Point out each Plasmodium parasite and each leukocyte.
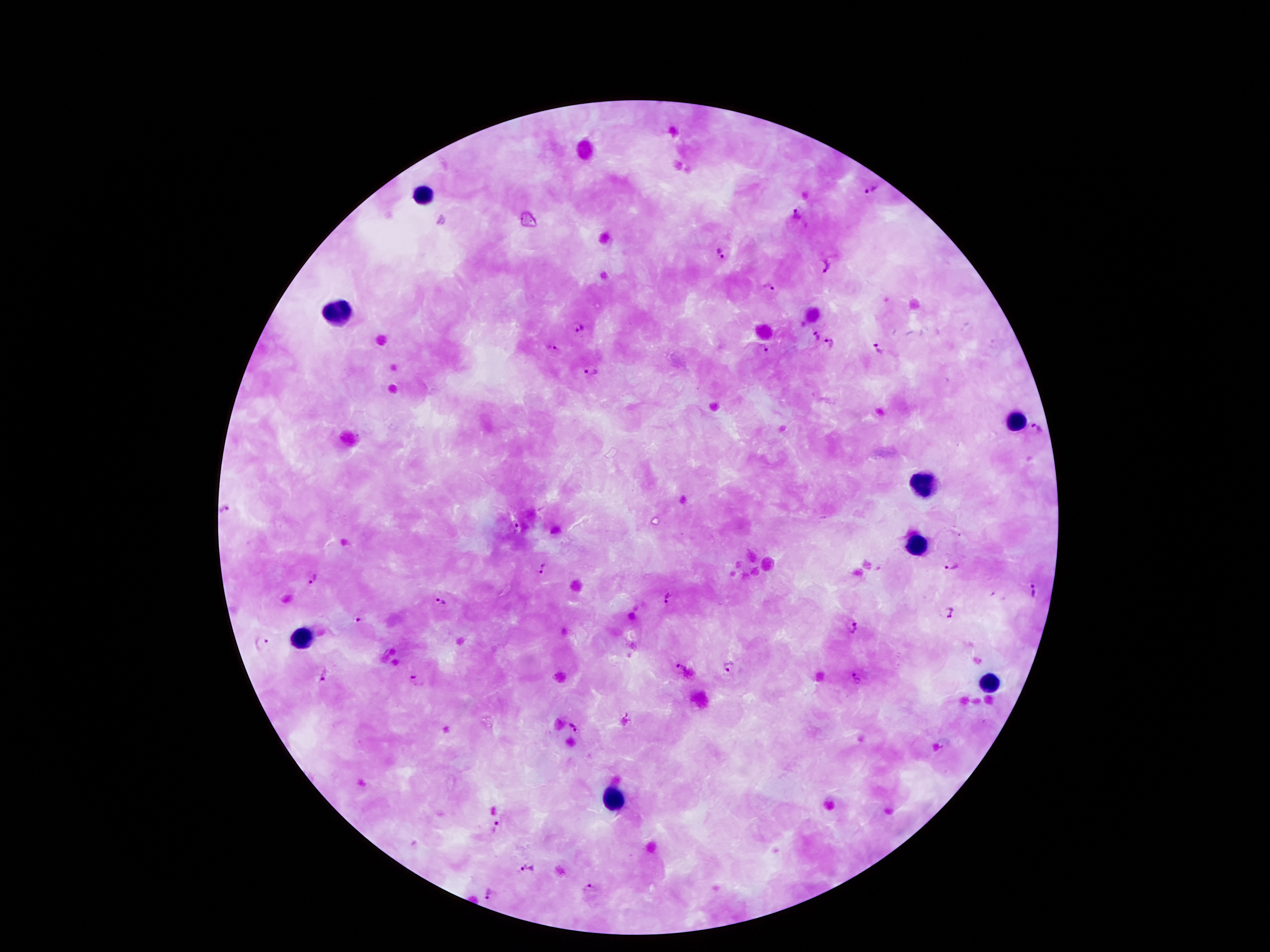
Approximate centers as (x, y) in pixels.
Plasmodium parasites: (871, 190), (796, 215), (720, 252), (823, 265), (767, 288), (579, 328), (815, 337), (831, 343), (763, 348), (551, 349), (876, 349), (593, 374), (1037, 431), (226, 510), (514, 529), (543, 566), (952, 566), (313, 577), (1034, 591), (669, 599), (442, 602), (947, 612), (359, 620), (854, 625), (262, 643), (730, 666), (679, 670), (323, 678), (418, 680), (575, 726), (495, 827), (527, 869), (589, 887), (491, 894).
Leukocytes: (425, 197), (336, 318), (1018, 422), (924, 483), (917, 545), (304, 637), (991, 681), (611, 800).

capture = smartphone through the microscope eyepiece
magnification = 100x
field of view = one from this slide
patient malaria status = infected with Plasmodium falciparum
stain = Giemsa
preparation = thick blood film
image size = 1270×952 pixels